Point out every malaria parasite and every leukocyte.
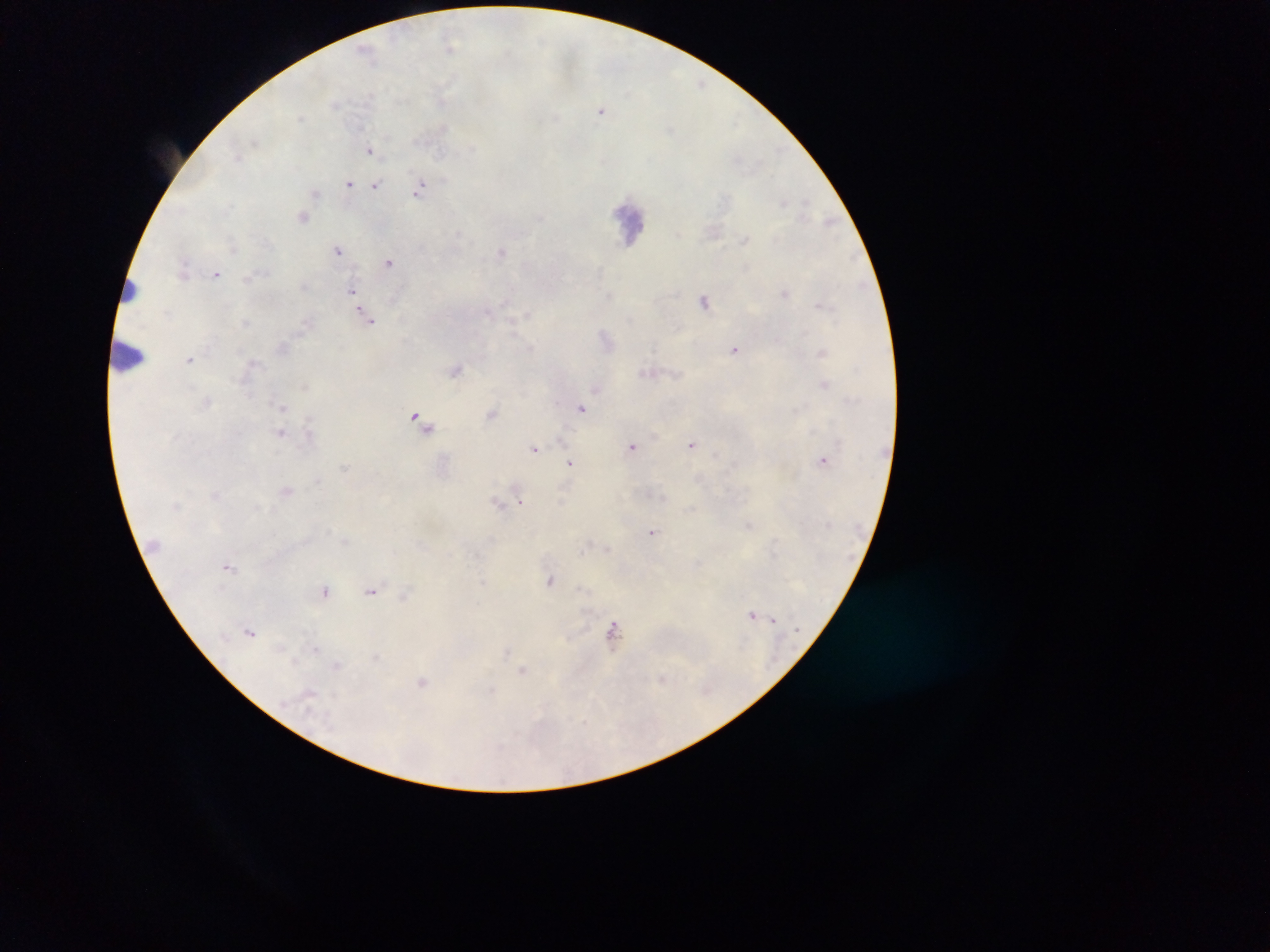
Approximate centers as x y in pixels.
Malaria parasites: 450 46; 701 83; 601 110; 370 150; 348 183; 376 185; 419 189; 315 194; 303 218; 338 249; 501 252; 389 262; 216 273; 352 291; 785 293; 705 301; 369 319; 735 349; 189 360; 456 369; 824 384; 582 408; 419 420; 692 444; 632 446; 535 448; 823 460; 570 463; 520 502; 499 504; 652 532; 229 566; 483 581; 550 581; 325 590; 371 590; 404 595; 751 614; 773 620; 250 631; 612 634; 280 648; 315 649; 295 662; 522 670; 662 679; 423 683; 309 693.
Leukocytes: 631 223; 128 290; 130 355.

Summary:
  - Preparation: thick blood film
  - Field of view: single
  - Country: Ghana
  - Capture: mobile-phone photograph through a microscope
  - Image size: 1270×952 pixels